Assess the morphology of the erythrocytes.
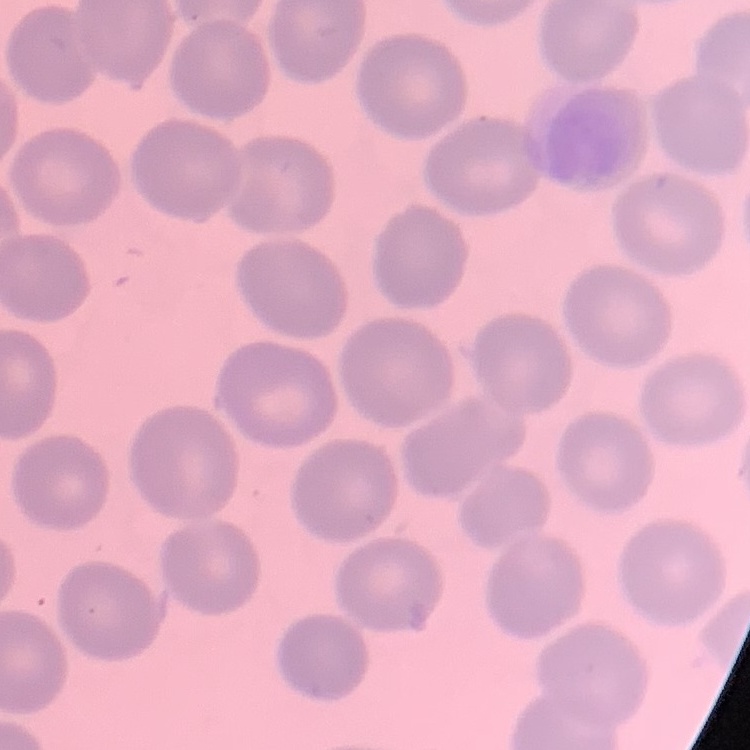

They show no rouleaux formation.

image type = square crop of a larger photomicrograph
preparation = thin blood film
stain = Field's or Giemsa